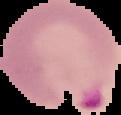

Image is 121×115 pixels. Malaria status: parasitized. From a thin blood smear. The area outside the segmented cell region is set to black.